Assess this cell for malaria.
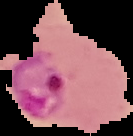
It is parasitized.

image type = segmented cell region on a black background
preparation = thin blood film
image size = 133×136 pixels